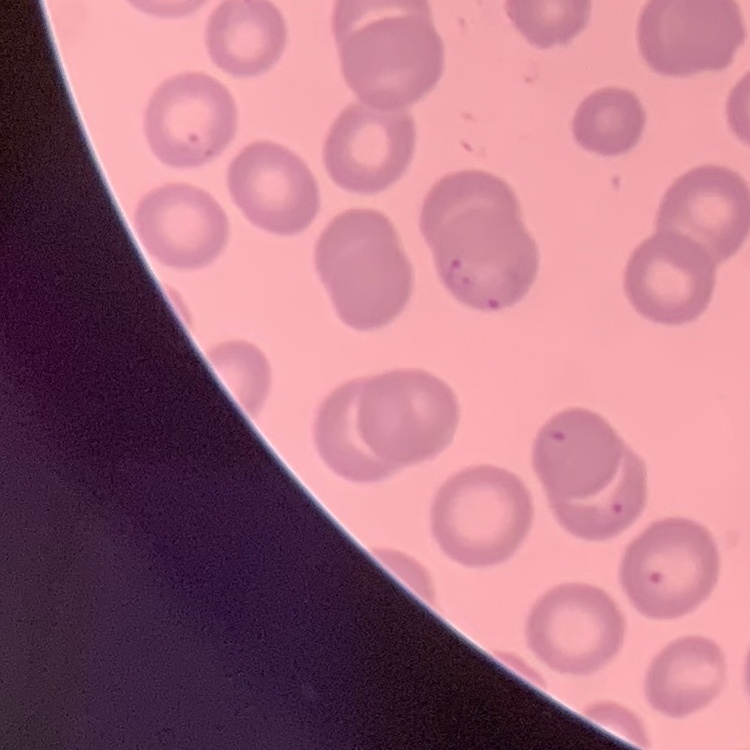
Summary:
  - Red blood cell morphology: no rouleaux formation
  - Preparation: thin blood film
  - Image type: square crop of a larger photomicrograph
  - Stain: Field's or Giemsa